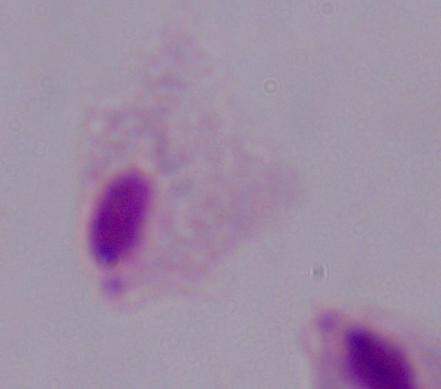
modality: micrograph
identification: trichomonad
magnification: 1000x